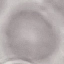
malaria status = uninfected
stain = Giemsa
preparation = thin smear
capture = smartphone through the microscope eyepiece
image type = cell patch, automatically extracted from a larger field of view and resized to 64 × 64 pixels